Identify the parasite.
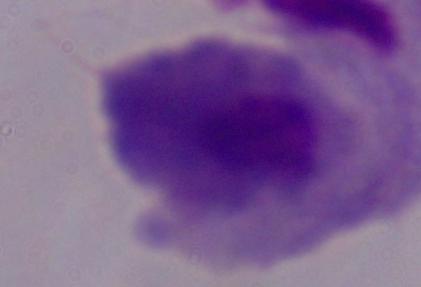
A trichomonad.

1000x magnification. Photomicrograph.